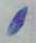

{
  "magnification": "1000x",
  "identification": "Toxoplasma gondii",
  "modality": "micrograph"
}